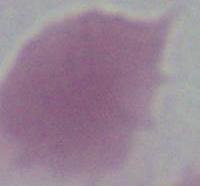

Summary:
  - Identification: erythrocyte
  - Magnification: 1000x
  - Modality: photomicrograph